Comment on the morphology of the red blood cells.
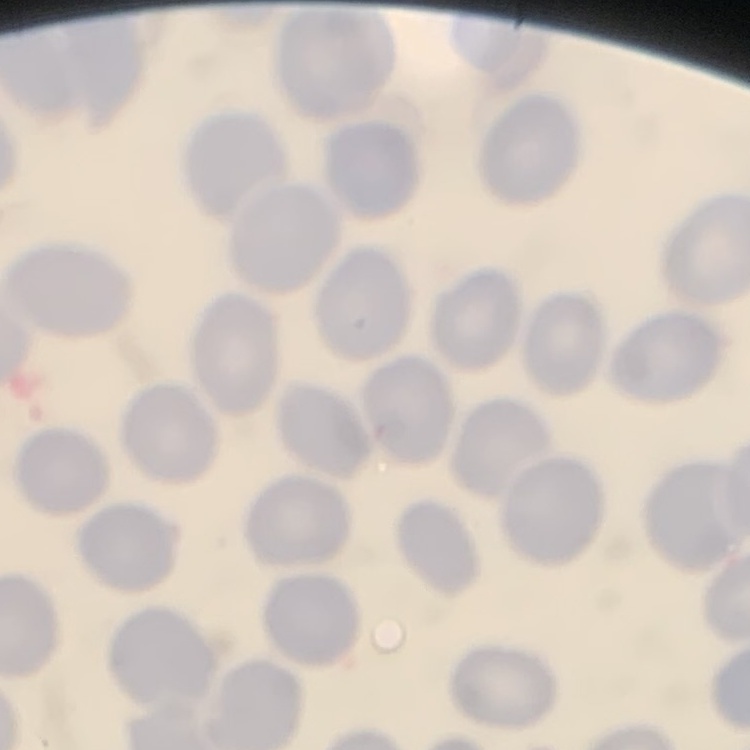
They show no rouleaux formation.

preparation: thin blood smear
image_type: one tile cut from a larger photomicrograph
stain: Field's or Giemsa